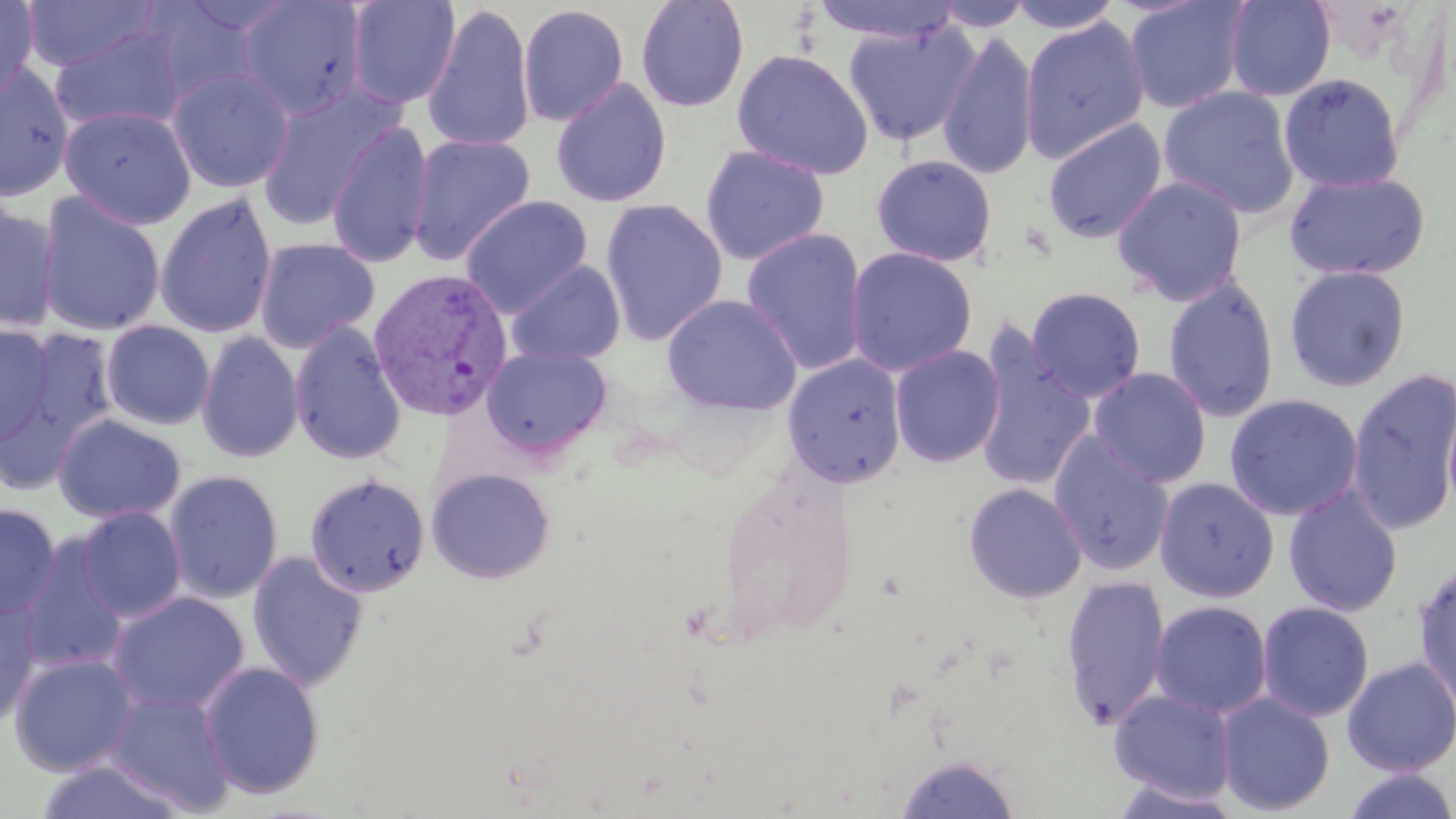 Approximate bounding boxes as (x1, y1, x2, y2) in pixels. Plasmodium vivax-infected red blood cell locations: (368, 266, 513, 422). Uninfected red blood cell locations: (0, 0, 39, 101), (237, 0, 368, 119), (345, 0, 461, 109), (635, 0, 750, 112), (810, 0, 964, 43), (932, 0, 1033, 32), (1005, 0, 1124, 34), (1124, 0, 1250, 114), (1223, 0, 1336, 101), (20, 1, 161, 72), (421, 3, 536, 153), (517, 3, 630, 126), (1020, 15, 1150, 164), (841, 21, 979, 147), (49, 24, 187, 134), (938, 29, 1040, 180), (731, 48, 873, 180), (0, 63, 76, 203), (166, 66, 295, 193), (1278, 72, 1406, 193), (550, 78, 673, 208), (255, 86, 401, 231), (1158, 86, 1299, 218), (59, 105, 197, 229), (1042, 117, 1168, 244), (327, 120, 434, 269), (407, 133, 536, 265), (700, 145, 830, 266), (870, 154, 998, 267), (1284, 169, 1432, 280), (1112, 174, 1248, 305), (37, 192, 166, 337), (154, 192, 278, 339), (460, 195, 594, 317), (600, 198, 728, 346), (0, 202, 60, 332), (741, 227, 869, 375), (254, 237, 380, 353), (845, 247, 978, 377), (506, 260, 625, 366), (1284, 264, 1412, 392), (1162, 274, 1280, 424), (1026, 286, 1147, 402), (661, 294, 802, 415), (289, 319, 407, 466), (101, 320, 215, 430), (0, 324, 55, 445), (15, 327, 118, 446), (196, 331, 304, 464), (973, 339, 1097, 492), (889, 344, 1006, 468), (481, 346, 612, 458), (781, 354, 907, 489), (1088, 367, 1212, 488), (1347, 367, 1456, 536), (1442, 382, 1456, 522), (1224, 393, 1364, 521), (53, 414, 186, 524), (1048, 432, 1175, 576), (426, 467, 556, 583), (164, 469, 283, 603), (304, 473, 431, 598), (1154, 477, 1279, 603), (962, 482, 1088, 604), (1283, 484, 1404, 617), (1, 502, 60, 620), (75, 506, 187, 622), (16, 537, 128, 676), (247, 550, 370, 693), (1413, 560, 1456, 713), (1059, 574, 1171, 729), (108, 591, 249, 715), (0, 595, 41, 728), (1149, 600, 1273, 718), (1256, 601, 1375, 722), (8, 652, 139, 776), (1341, 656, 1456, 776), (198, 661, 325, 799), (1109, 689, 1238, 804), (105, 690, 235, 815), (1215, 692, 1335, 816), (894, 753, 1020, 818), (35, 759, 187, 819), (1341, 768, 1456, 819), (1106, 778, 1245, 819). Slide-level diagnosis: Plasmodium vivax. Thin blood film. Captured at 1000x magnification. Image is 1456×819 pixels. Optical microscopy. Single field of view. May-Grünwald-Giemsa-stained preparation.